Locate every Trypanosoma brucei.
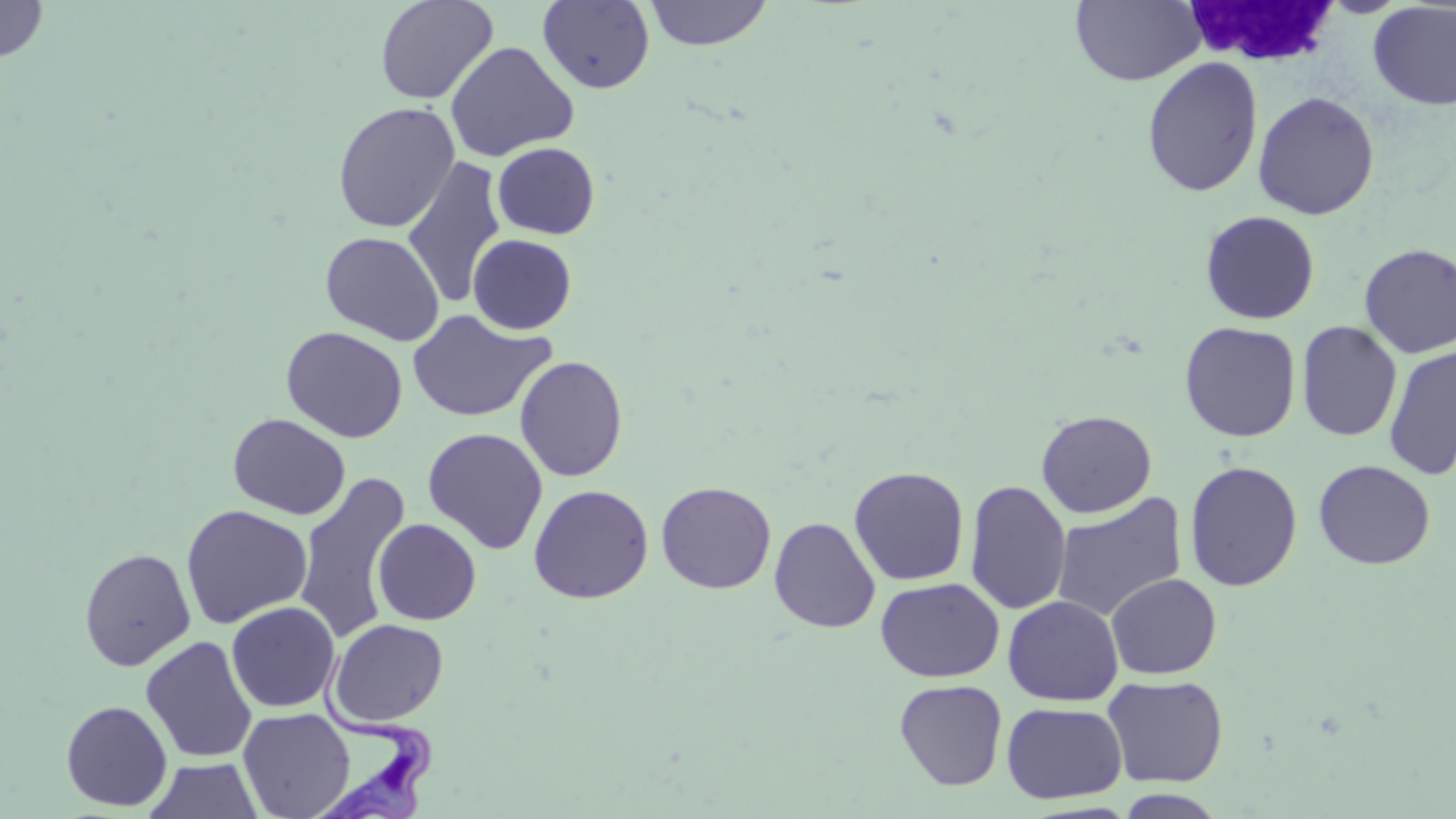
Approximate bounding boxes as [x1, y1, x2, y2] in pixels.
Trypanosoma brucei: [309, 650, 437, 818].

slide-level diagnosis = Trypanosoma brucei
field of view = single
image size = 1456×819 pixels
uninfected red blood cell locations = approximate bounding boxes as [x1, y1, x2, y2] in pixels: [0, 0, 49, 63], [375, 0, 498, 105], [644, 0, 773, 51], [1071, 0, 1205, 86], [537, 1, 655, 94], [1368, 2, 1456, 110], [445, 41, 579, 162], [1141, 56, 1264, 198], [1253, 91, 1379, 220], [332, 103, 460, 232], [492, 142, 600, 239], [401, 156, 507, 310], [1200, 210, 1320, 324], [320, 231, 445, 345], [467, 234, 577, 335], [1359, 244, 1456, 359], [406, 309, 554, 423], [1296, 320, 1402, 442], [1179, 321, 1301, 442], [281, 326, 408, 443], [1384, 344, 1456, 480], [514, 354, 628, 482], [1036, 409, 1157, 518], [228, 414, 351, 520], [422, 427, 548, 554], [1313, 459, 1436, 569], [1184, 460, 1303, 592], [848, 466, 969, 586], [293, 472, 412, 645], [965, 480, 1071, 615], [656, 481, 776, 594], [528, 484, 654, 604], [1051, 492, 1188, 622], [180, 504, 312, 628], [769, 516, 880, 633], [372, 518, 481, 625], [78, 547, 196, 671], [1105, 572, 1222, 679], [875, 578, 1004, 682], [1003, 595, 1123, 706], [226, 601, 341, 712], [328, 618, 449, 726], [141, 635, 258, 763], [1102, 674, 1229, 788], [894, 679, 1008, 791], [60, 700, 173, 811], [1001, 701, 1127, 804], [237, 707, 355, 819], [145, 758, 262, 817], [1115, 790, 1229, 818]
white blood cell locations = approximate bounding boxes as [x1, y1, x2, y2] in pixels: [1179, 1, 1346, 69]
modality = optical microscopy
stain = May-Grünwald-Giemsa
preparation = thin blood smear
magnification = 1000x